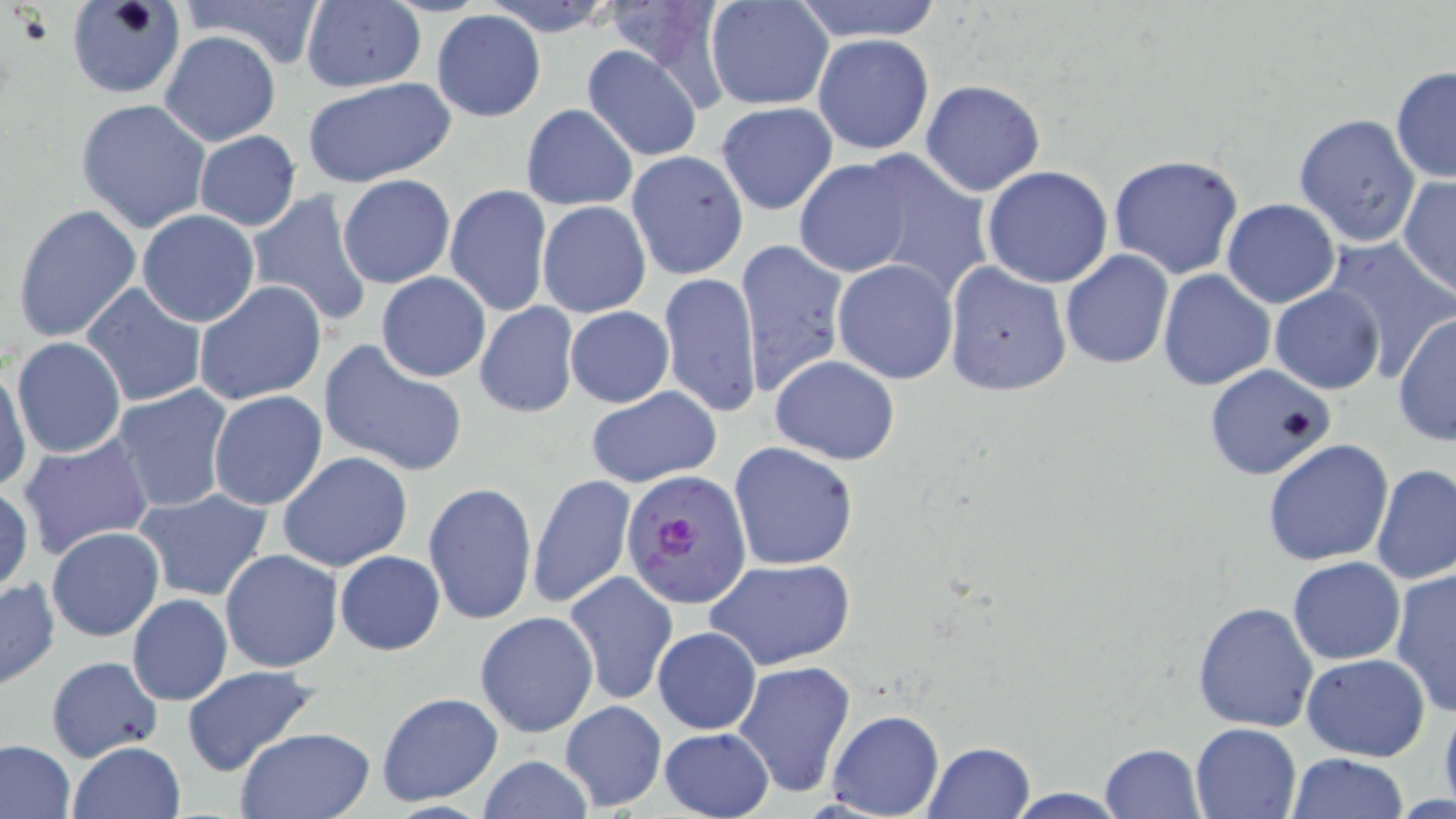
Summary:
  - Coordinate format: approximate bounding boxes as (x1,y1)-(x2,y2) corner pairs in pixels
  - Uninfected red blood cell locations: (68,0)-(185,100), (171,0)-(327,70), (480,0)-(620,35), (705,0)-(835,110), (789,0)-(945,43), (299,1)-(427,93), (432,9)-(547,123), (160,30)-(281,146), (813,34)-(934,156), (581,44)-(705,162), (1390,66)-(1456,184), (302,77)-(456,188), (920,79)-(1045,197), (75,98)-(213,235), (715,101)-(838,216), (521,104)-(638,210), (1293,113)-(1420,249), (194,130)-(301,231), (625,150)-(750,282), (850,150)-(993,301), (1109,154)-(1246,279), (792,158)-(916,277), (981,166)-(1114,288), (337,174)-(456,289), (1397,176)-(1456,299), (445,184)-(553,317), (248,190)-(373,327), (1222,198)-(1341,308), (11,201)-(143,344), (537,201)-(651,318), (136,209)-(261,328), (1319,235)-(1455,378), (736,239)-(849,396), (1060,250)-(1173,369), (832,258)-(959,385), (943,260)-(1073,396), (1156,270)-(1275,391), (375,271)-(491,383), (658,273)-(763,418), (193,280)-(329,406), (78,284)-(208,407), (1269,285)-(1385,394), (473,303)-(579,417), (565,306)-(673,407), (1393,313)-(1455,448), (12,336)-(125,458), (319,338)-(470,478), (768,356)-(898,464), (1,363)-(30,493), (1203,364)-(1337,481), (110,384)-(236,515), (585,387)-(722,490), (207,390)-(328,511), (16,434)-(155,559), (1262,438)-(1394,567), (729,442)-(859,570), (280,452)-(413,571), (1370,465)-(1456,586), (527,472)-(636,610), (424,481)-(538,623), (0,485)-(34,595), (134,488)-(275,602), (46,527)-(164,642), (220,549)-(343,673), (334,551)-(445,655), (1287,556)-(1406,666), (706,558)-(853,671), (1390,564)-(1456,718), (564,570)-(678,707), (1,577)-(60,689), (127,594)-(233,705), (1193,601)-(1319,731), (475,611)-(600,739), (652,627)-(762,735), (1301,652)-(1430,761), (45,655)-(163,763), (732,661)-(856,798), (181,665)-(320,777), (375,691)-(504,807), (1436,695)-(1456,809), (558,701)-(667,813), (826,709)-(944,819), (1189,722)-(1303,818), (234,727)-(375,818), (659,727)-(773,819), (0,739)-(76,819), (67,740)-(185,819), (923,741)-(1035,818), (1100,741)-(1207,817), (1285,753)-(1410,818), (476,756)-(595,818), (998,789)-(1133,818)
  - Plasmodium falciparum-infected red blood cell locations: (622,471)-(750,609)
  - Slide-level diagnosis: Plasmodium falciparum
  - Magnification: 1000x
  - Preparation: thin blood smear
  - Image size: 1456×819 pixels
  - Stain: May-Grünwald-Giemsa
  - Modality: light microscopy
  - Field of view: one of a larger specimen